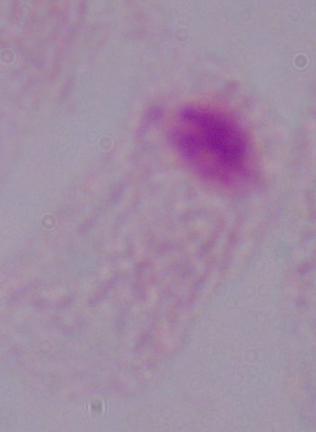
{
  "modality": "photomicrograph",
  "identification": "trichomonad",
  "magnification": "1000x"
}